Assess this cell for malaria.
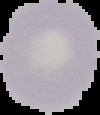
Uninfected.

Summary:
  - Image size: 100×115 pixels
  - Image type: segmented cell region with the area outside set to black
  - Preparation: thin blood smear